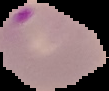
Summary:
  - Image type: segmented cell region with the area outside set to black
  - Result: Plasmodium parasites detected
  - Image size: 109×91 pixels
  - Preparation: thin blood smear